Classify this cell by malaria status.
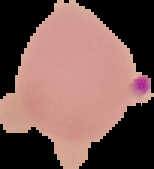
Parasitized.

image_type: segmented cell region with the area outside set to black
preparation: thin blood film
image_size: 154×169 pixels